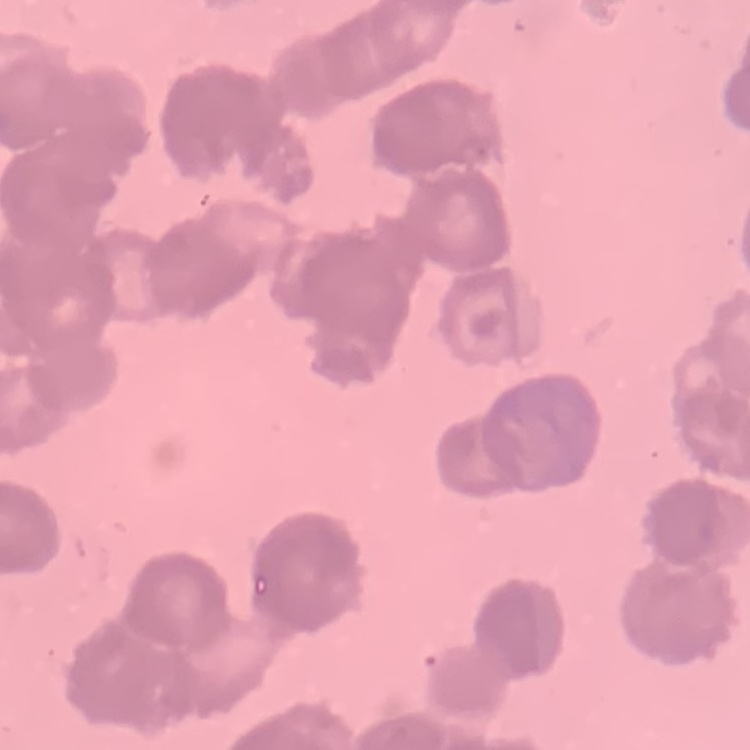
Summary:
  - Red blood cell morphology: rouleaux formation
  - Stain: Field's or Giemsa
  - Preparation: thin blood smear
  - Image type: one tile cut from a larger photomicrograph